Locate and identify every blood parasite.
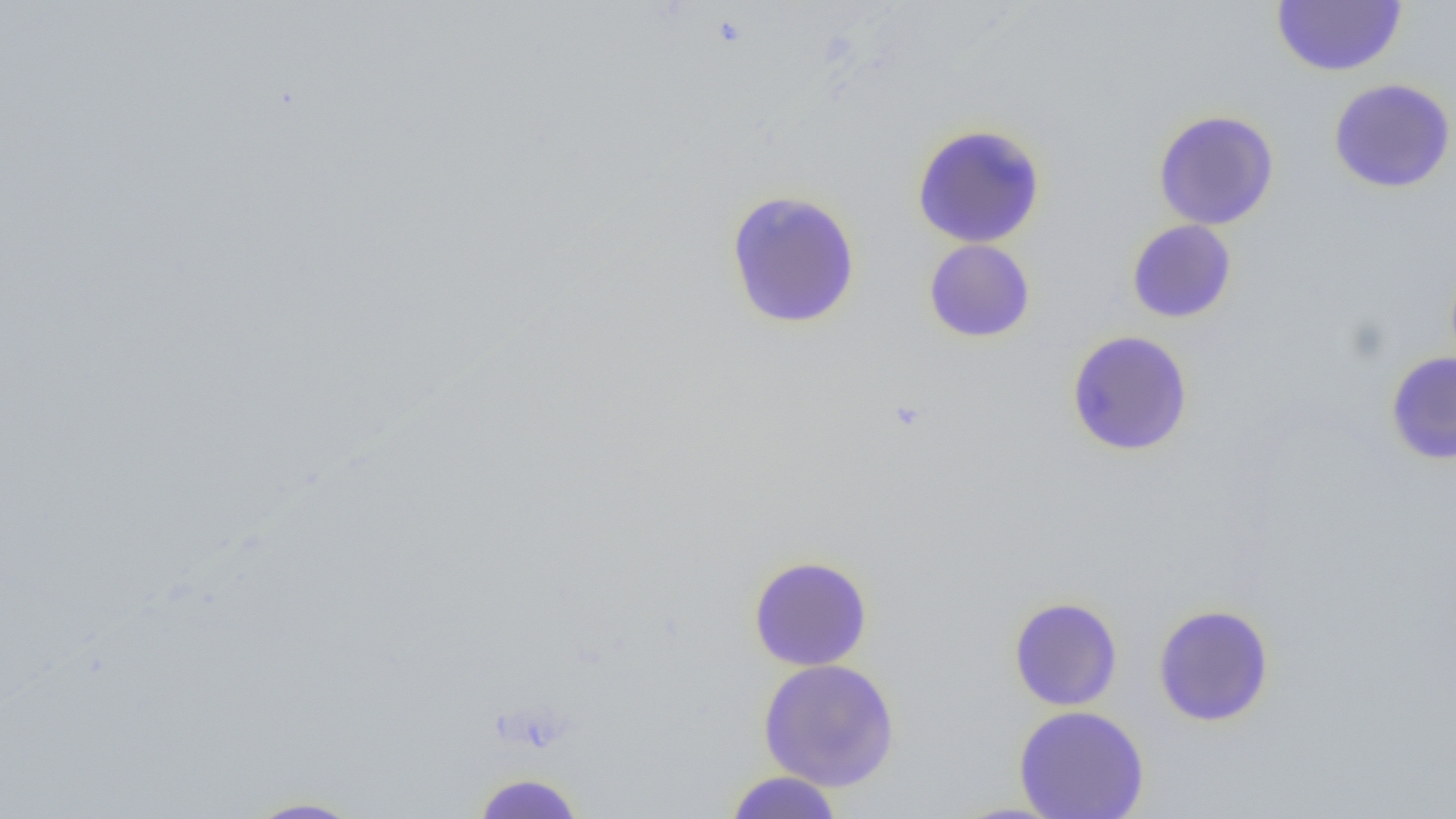

No blood parasites observed.

slide-level diagnosis = negative for blood parasites
modality = light microscopy
image size = 1456×819 pixels
preparation = thin blood film
uninfected red blood cell locations = approximate bounding boxes as (x1, y1, x2, y2) in pixels: (1271, 0, 1408, 76), (1328, 78, 1455, 193), (1152, 110, 1280, 230), (911, 124, 1046, 249), (725, 189, 862, 330), (1126, 219, 1237, 323), (923, 239, 1036, 343), (1066, 329, 1194, 457), (1385, 352, 1456, 465), (747, 555, 873, 671), (1008, 596, 1123, 711), (1152, 604, 1275, 727), (758, 658, 901, 792), (1013, 705, 1150, 819), (723, 771, 845, 818), (469, 772, 588, 817), (236, 795, 372, 818)
field of view = one of a larger specimen
magnification = 1000x